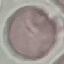
malaria status = uninfected
preparation = thin smear
capture = smartphone camera at the microscope eyepiece
stain = Giemsa
image type = cell patch, automatically extracted from a larger field of view and resized to 64 × 64 pixels